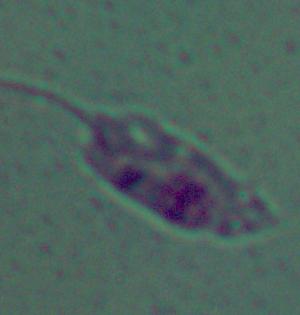
{
  "magnification": "1000x",
  "modality": "photomicrograph",
  "identification": "Leishmania"
}